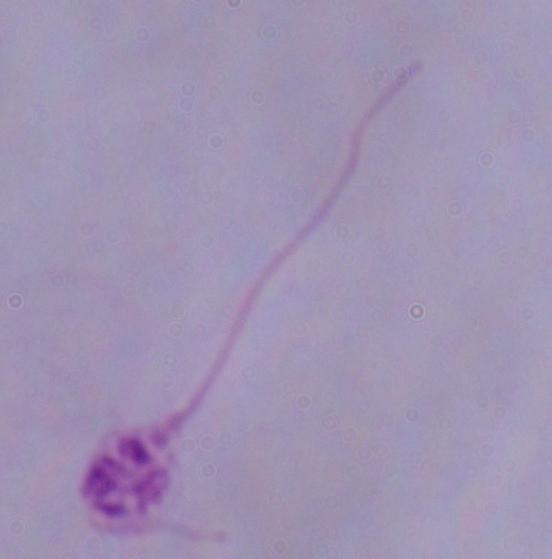

magnification = 1000x
identification = Leishmania
modality = micrograph